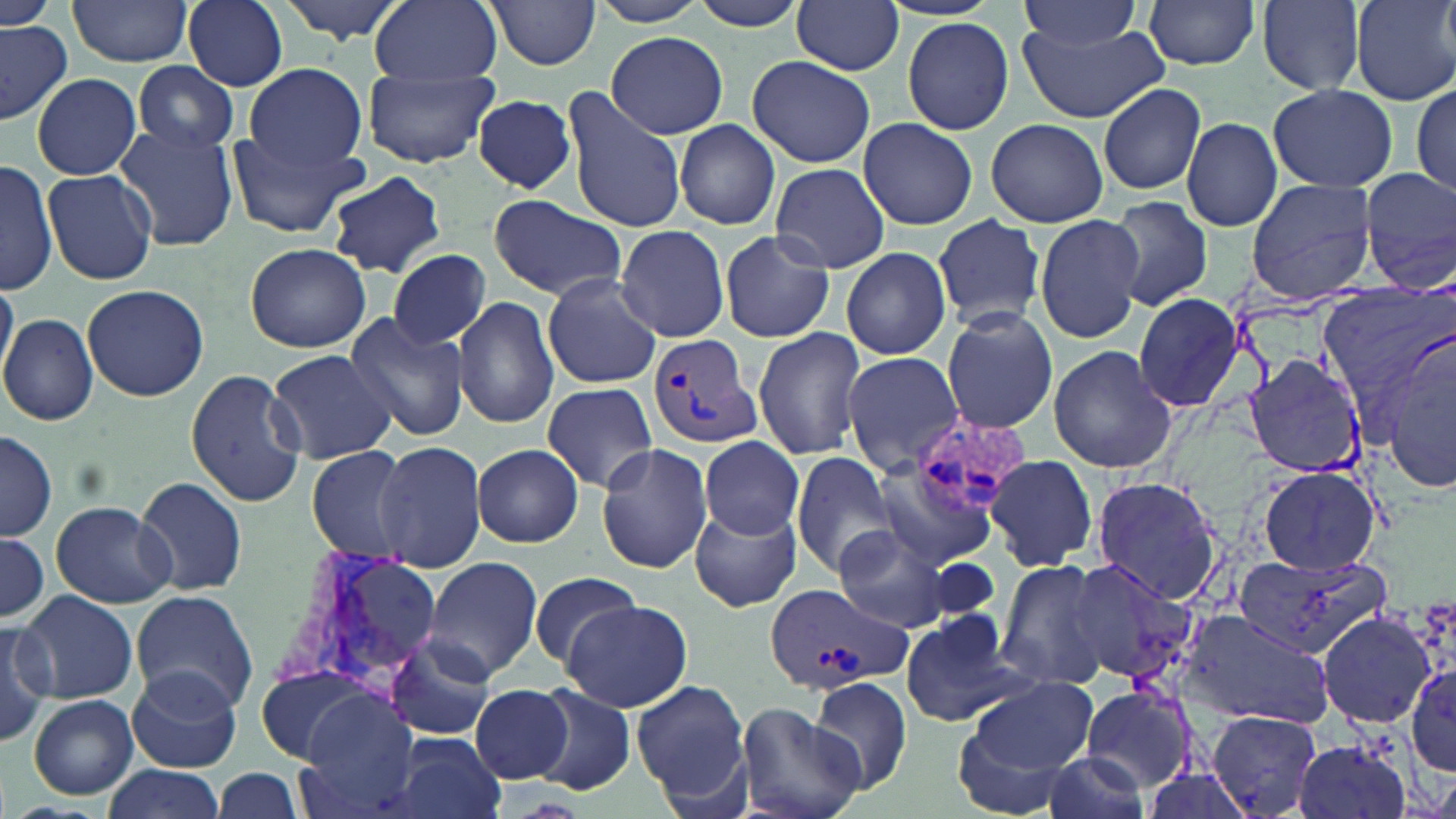
Approximate bounding boxes as (x1,y1)-(x2,y2) corner pairs in pixels. Uninfected red blood cell locations: (67,0)-(195,67), (184,0)-(289,90), (277,0)-(410,43), (369,0)-(502,86), (590,0)-(713,27), (684,0)-(813,31), (791,0)-(906,74), (1143,0)-(1262,71), (1352,0)-(1455,105), (1,1)-(53,31), (488,1)-(599,70), (1016,1)-(1147,53), (1258,1)-(1367,96), (901,15)-(1015,135), (1018,19)-(1170,124), (0,21)-(74,121), (605,31)-(729,139), (746,56)-(875,168), (132,61)-(238,155), (244,63)-(368,171), (362,67)-(500,168), (31,73)-(142,180), (1413,77)-(1455,198), (1097,82)-(1206,195), (1268,84)-(1397,193), (560,88)-(688,234), (472,94)-(577,193), (1181,115)-(1282,233), (985,117)-(1108,227), (856,118)-(978,230), (675,120)-(780,232), (114,125)-(238,252), (224,128)-(373,237), (0,159)-(57,296), (770,162)-(888,274), (1359,169)-(1455,287), (42,170)-(156,285), (327,171)-(446,278), (1245,178)-(1378,304), (486,193)-(626,303), (1103,196)-(1212,312), (1036,212)-(1143,343), (931,216)-(1050,331), (616,224)-(731,343), (717,230)-(836,343), (245,243)-(371,352), (842,246)-(952,360), (388,249)-(492,351), (541,274)-(662,390), (0,276)-(18,381), (81,284)-(209,401), (1317,285)-(1453,408), (1131,291)-(1247,415), (454,294)-(559,429), (941,308)-(1059,433), (341,311)-(472,441), (0,313)-(98,425), (752,327)-(869,463), (1378,329)-(1456,497), (1047,346)-(1176,473), (266,349)-(398,464), (839,351)-(963,477), (1243,354)-(1368,479), (186,368)-(305,507), (541,382)-(658,492), (1,431)-(57,543), (698,437)-(805,540), (375,439)-(487,572), (473,442)-(583,547), (595,443)-(714,574), (301,445)-(414,561), (790,452)-(904,579), (984,453)-(1097,572), (1254,465)-(1383,574), (871,466)-(997,571), (135,477)-(248,598), (1090,477)-(1226,606), (50,502)-(177,608), (690,506)-(801,612), (831,525)-(956,634), (0,532)-(49,628), (1236,551)-(1391,661), (424,557)-(544,682), (994,558)-(1106,691), (1063,558)-(1198,683), (529,570)-(641,673), (130,589)-(258,715), (19,590)-(137,704), (561,599)-(691,711), (1175,607)-(1333,729), (898,609)-(1035,730), (1315,609)-(1438,729), (0,619)-(54,747), (385,632)-(499,743), (250,661)-(382,764), (1406,662)-(1455,776), (126,665)-(242,773), (810,677)-(912,795), (967,678)-(1098,778), (632,679)-(752,809), (471,683)-(574,783), (1079,683)-(1198,792), (529,685)-(634,795), (293,693)-(423,816), (28,694)-(139,800), (734,700)-(864,819), (1206,710)-(1323,817), (950,714)-(1086,818), (388,734)-(506,819), (1292,734)-(1412,819), (1041,751)-(1153,819), (101,764)-(224,819), (212,767)-(306,819). Plasmodium vivax-infected red blood cell locations: (646,332)-(763,451), (909,410)-(1030,518), (280,546)-(416,697), (763,581)-(914,695). Slide-level diagnosis: Plasmodium vivax. Optical microscopy. Image is 1456×819 pixels. 1000x magnification. May-Grünwald-Giemsa-stained preparation. One field of a larger specimen. Thin blood film.